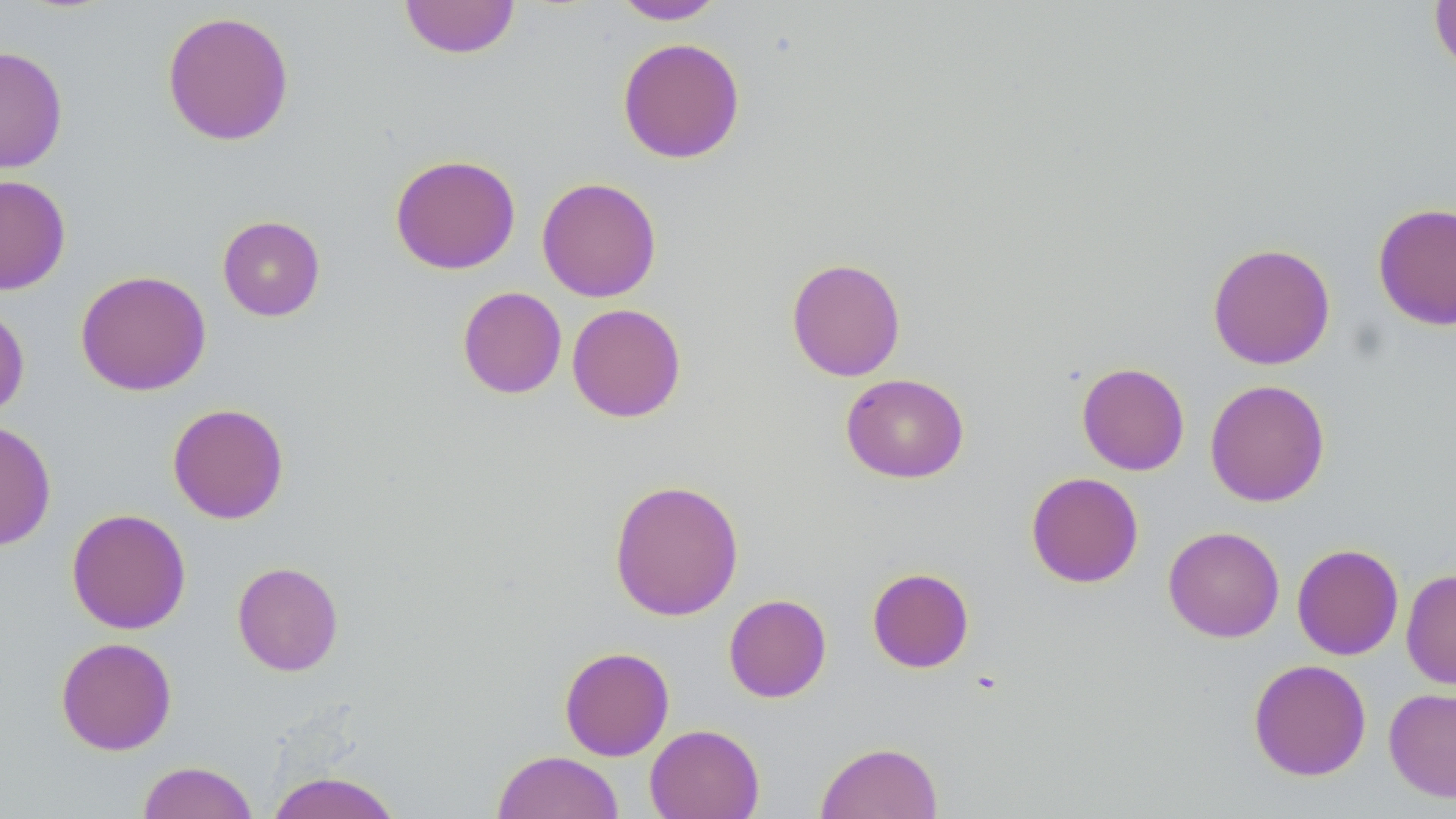

Summary:
  - Coordinate format: approximate bounding boxes as (x1, y1, x2, y2) in pixels
  - Uninfected red blood cell locations: (399, 0, 521, 59), (611, 0, 727, 25), (1429, 0, 1456, 79), (161, 10, 295, 146), (617, 37, 746, 164), (0, 46, 69, 174), (389, 154, 521, 275), (0, 174, 71, 295), (536, 176, 662, 303), (1372, 202, 1456, 331), (216, 215, 326, 321), (1207, 242, 1335, 370), (786, 257, 906, 381), (75, 269, 211, 396), (457, 286, 567, 399), (0, 300, 30, 420), (566, 303, 686, 423), (1076, 362, 1190, 475), (840, 373, 969, 483), (1205, 379, 1330, 507), (167, 403, 289, 524), (0, 419, 57, 552), (1026, 471, 1144, 588), (608, 478, 744, 621), (66, 508, 191, 635), (1163, 526, 1285, 642), (1292, 543, 1404, 660), (232, 561, 344, 676), (867, 567, 975, 673), (1401, 568, 1456, 690), (723, 594, 832, 703), (55, 636, 177, 755), (559, 646, 674, 761), (1248, 659, 1371, 781), (1384, 687, 1456, 802), (645, 724, 764, 819), (815, 741, 943, 818), (492, 750, 625, 819), (136, 760, 258, 819), (266, 771, 403, 819)
  - Slide-level diagnosis: no evidence of blood parasites
  - Magnification: 1000x
  - Image size: 1456×819 pixels
  - Preparation: thin blood film
  - Field of view: single
  - Stain: May-Grünwald-Giemsa
  - Modality: optical microscopy